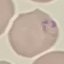

Summary:
  - Result: malaria parasites detected
  - Image type: automatically extracted cell patch, resized to 64 × 64 pixels
  - Stain: Giemsa
  - Capture: smartphone camera at the microscope eyepiece
  - Preparation: thin smear